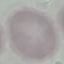

Summary:
  - Result: negative for malaria parasites
  - Capture: smartphone through the microscope eyepiece
  - Image type: cell patch, automatically extracted from a larger field of view and resized to 64 × 64 pixels
  - Stain: Giemsa
  - Preparation: thin smear